Report the malaria status of this cell.
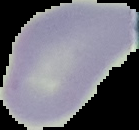

It is uninfected.

From a thin blood smear. The area outside the segmented cell region is set to black. Image is 139×130 pixels.